Report the malaria status of this cell.
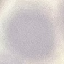
Uninfected.

Thin blood smear. Acquired by smartphone through the microscope eyepiece. Giemsa-stained preparation. Automatically extracted cell patch, resized to 64 × 64 pixels.